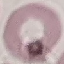
Summary:
  - Malaria status: uninfected
  - Stain: Giemsa
  - Preparation: thin blood film
  - Image type: automatically extracted cell patch, resized to 64 × 64 pixels
  - Capture: smartphone camera at the microscope eyepiece